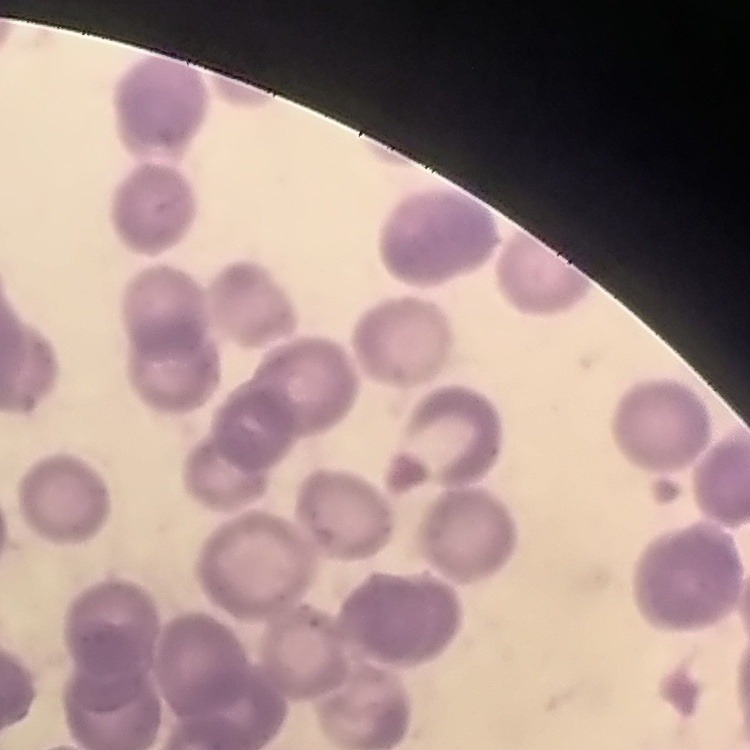 The erythrocytes exhibit rouleaux formation. Square crop of a larger photomicrograph. Thin blood smear. Field's or Giemsa stain.